Find the cells and give the type of each one.
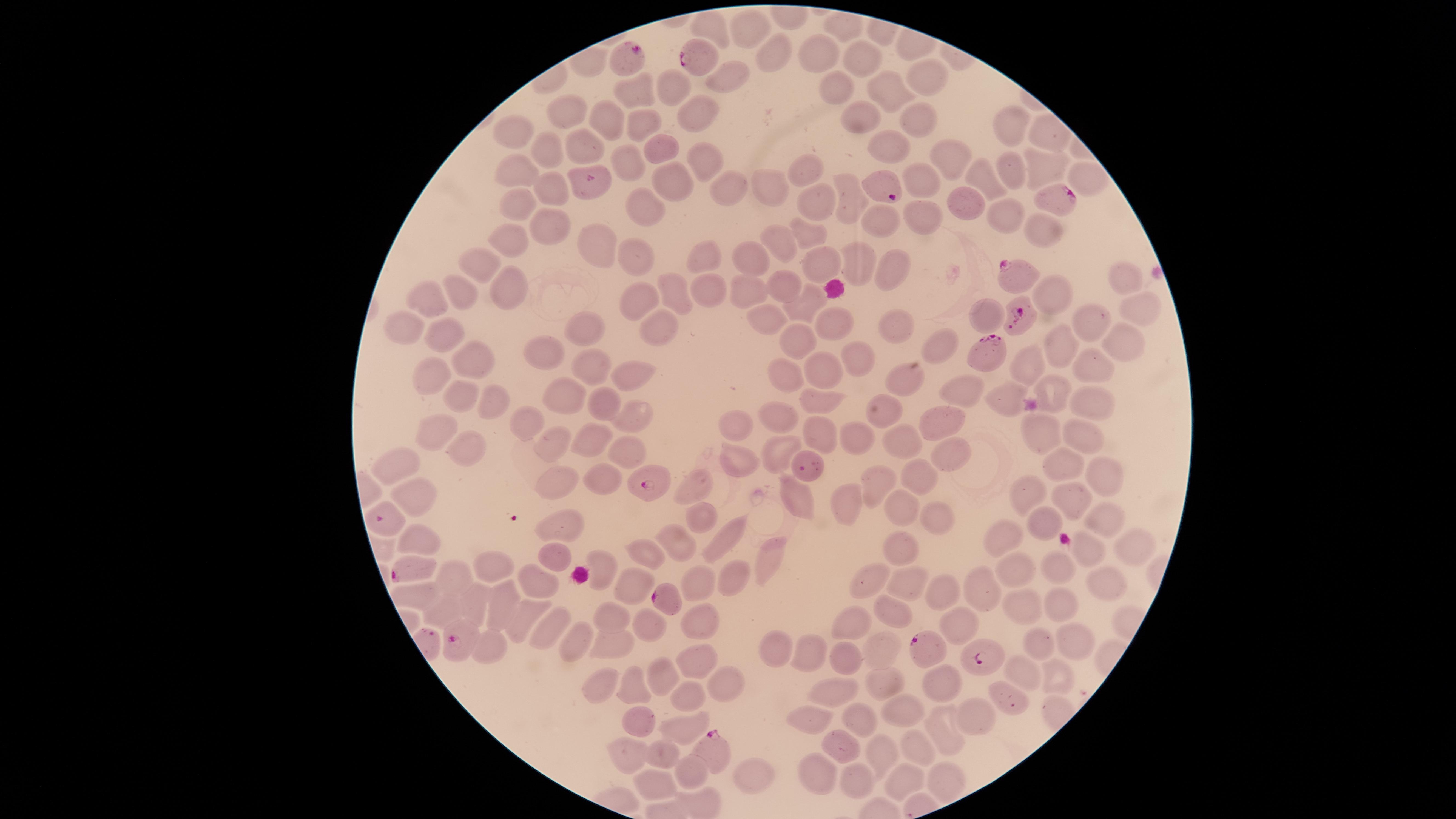
Approximate marker points as [x, y] in pixels.
Parasitized red blood cells: [699, 59], [626, 60], [1060, 197], [1015, 274], [1015, 318], [988, 353], [645, 480], [412, 571], [665, 599], [459, 636], [920, 647], [983, 659], [714, 754].
Uninfected red blood cells: [751, 25], [716, 29], [822, 53], [767, 55], [864, 56], [920, 71], [731, 76], [677, 88], [638, 91], [885, 91], [837, 94], [565, 107], [696, 113], [862, 114], [608, 117], [919, 118], [638, 125], [1012, 126], [518, 132], [891, 142], [578, 144], [657, 144], [551, 146], [950, 157], [706, 160], [516, 162], [627, 166], [1011, 166], [805, 168], [1048, 170], [1084, 173], [920, 179], [666, 180], [984, 184], [544, 187], [766, 189], [724, 190], [847, 198], [959, 201], [816, 203], [647, 208], [527, 209], [998, 214], [921, 216], [877, 221], [545, 223], [1037, 227], [811, 233], [512, 241], [780, 241], [599, 245], [699, 255], [639, 260], [821, 260], [855, 260], [754, 261], [481, 263], [895, 272], [1122, 278], [502, 286], [777, 286], [748, 287], [462, 288], [705, 293], [813, 294], [677, 295], [1055, 297], [428, 300], [645, 303], [1134, 308], [764, 313], [984, 317], [1091, 322], [410, 323], [891, 323], [833, 325], [441, 327], [580, 328], [656, 331], [801, 340], [936, 343], [1057, 344], [1122, 344], [471, 351], [540, 353], [1024, 360], [859, 361], [1087, 364], [588, 366], [821, 366], [639, 373], [784, 373], [426, 374], [900, 380], [1056, 387], [462, 392], [959, 392], [562, 394], [1091, 398], [1000, 400], [606, 403], [817, 403], [484, 404], [884, 408], [637, 414], [772, 415], [944, 420], [739, 422], [524, 425], [436, 426], [1032, 434], [1081, 434], [823, 436], [862, 438], [904, 442], [596, 443], [556, 444], [471, 449], [622, 451], [780, 451], [950, 454], [736, 458], [400, 462], [1062, 463], [1102, 470], [912, 476], [558, 478], [597, 480], [880, 483], [697, 486], [1028, 486], [793, 491], [407, 496], [1064, 500], [846, 504], [899, 506], [701, 514], [938, 515], [1095, 517], [1043, 521], [562, 528], [412, 535], [1004, 539], [1129, 539], [722, 540], [675, 543], [899, 549], [646, 551], [1091, 551], [551, 556], [765, 556], [604, 564], [492, 567], [1024, 570], [1064, 570], [730, 575], [1097, 576], [457, 578], [538, 581], [695, 581], [872, 582], [907, 585], [633, 586], [423, 592], [945, 593], [983, 593], [501, 598], [1056, 601], [473, 603], [1019, 607], [442, 610], [896, 610], [527, 616], [612, 618], [696, 619], [953, 621], [656, 625], [545, 626], [850, 630], [575, 636], [1029, 639], [612, 641], [489, 644], [1073, 644], [875, 647], [777, 649], [805, 652], [842, 659], [697, 664], [1061, 672], [656, 675], [1031, 676], [627, 682], [717, 682], [598, 683], [884, 684], [946, 687], [829, 690], [686, 696], [1008, 697], [901, 706], [976, 711], [638, 718], [858, 719], [806, 721], [685, 727], [938, 728], [920, 747], [659, 750], [843, 751], [631, 754], [881, 755], [690, 766], [816, 773], [752, 775], [899, 777], [941, 779], [852, 780], [652, 782].
No white blood cells identified.

species: Plasmodium falciparum
field_of_view: single
capture: smartphone photograph through the microscope eyepiece
visible_region: circular
preparation: thin blood smear
stain: Giemsa
image_size: 1456×819 pixels